Give the preparation type.
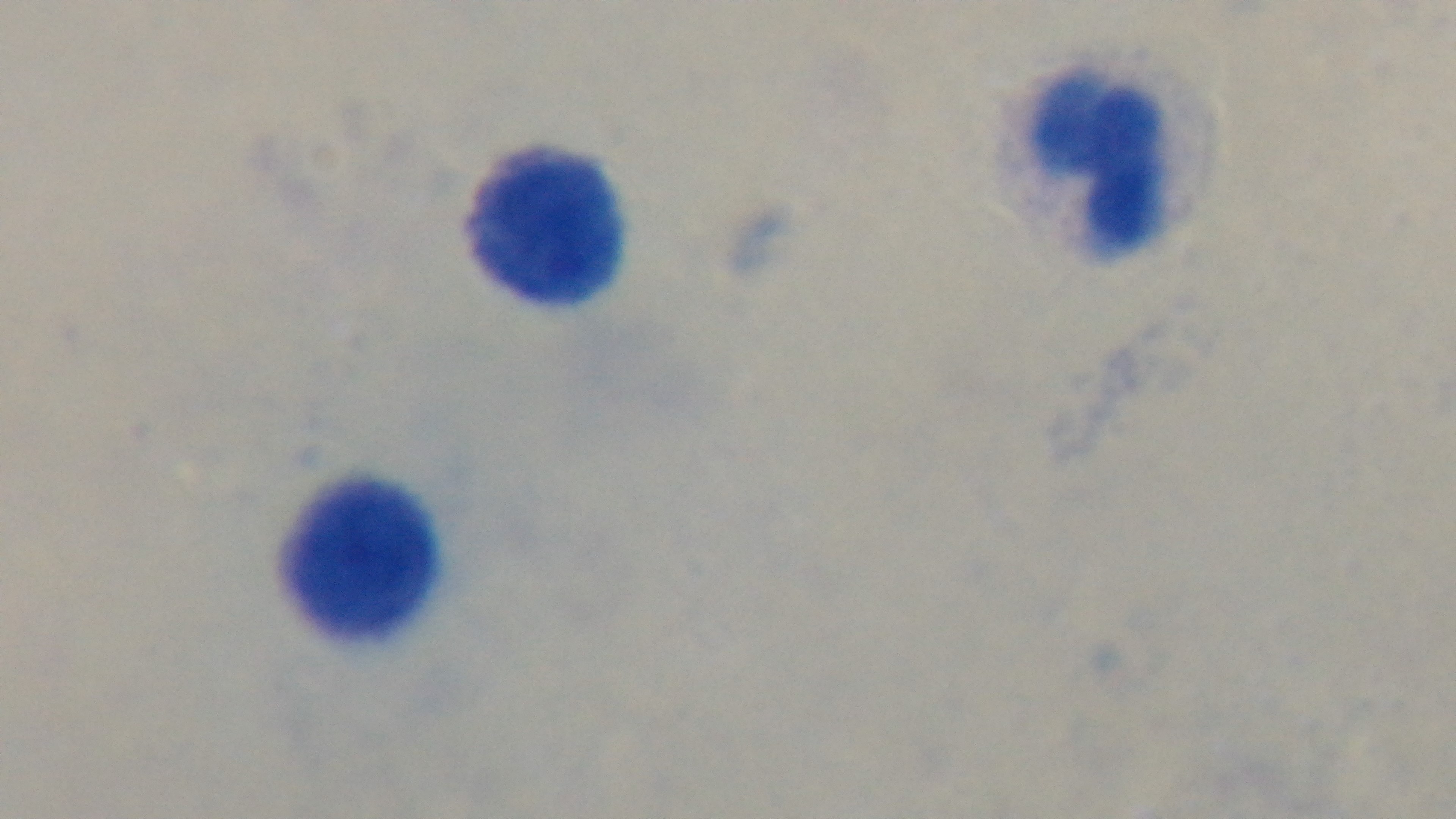
It is a thick blood film.

Mounted 4K digital camera. Giemsa stain. Malaria status: negative. Oil-immersion objective, 100x. Light microscopy. Single field of view.